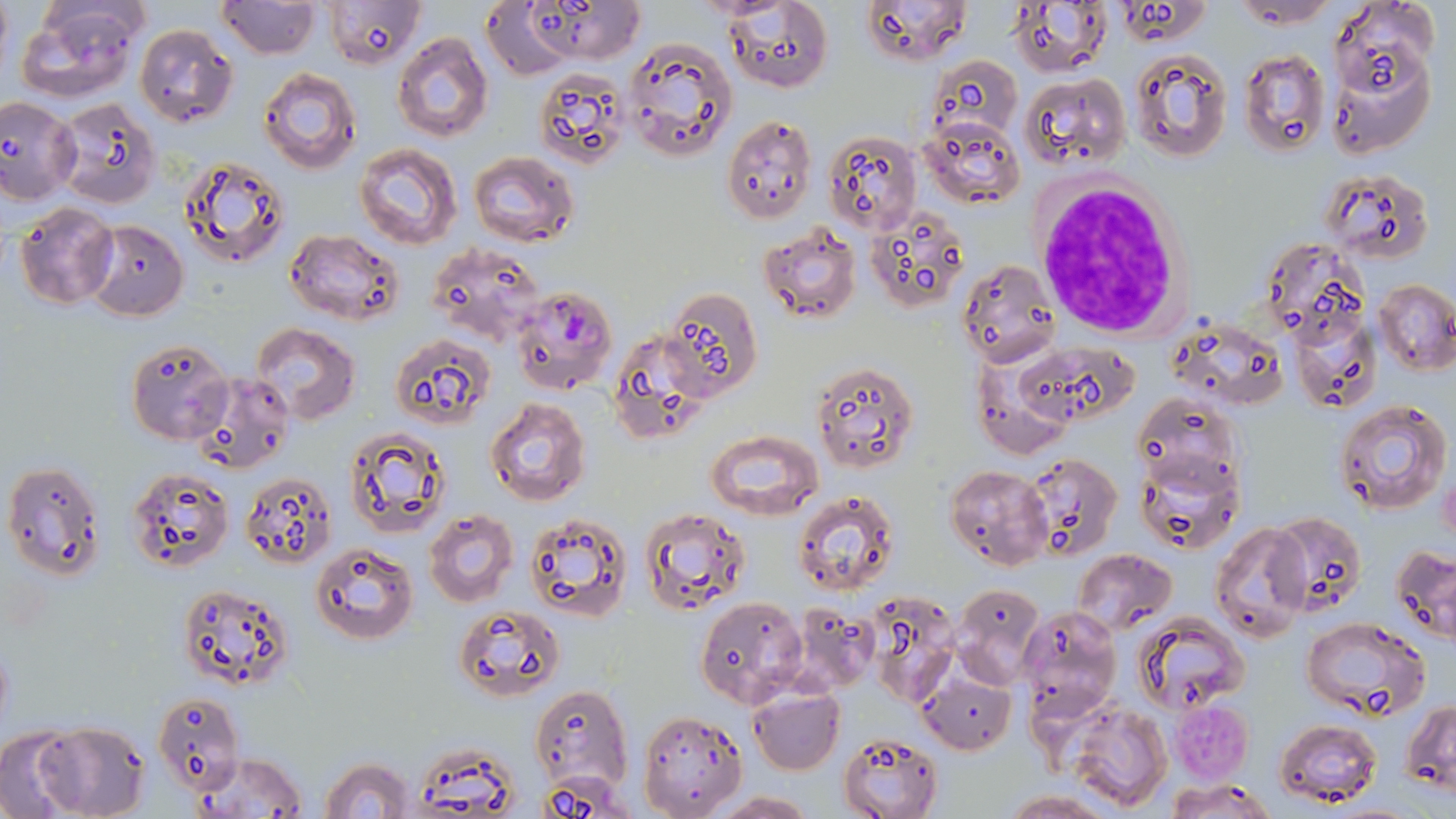

slide-level diagnosis = Plasmodium falciparum
field of view = one of a larger specimen
magnification = 1000x
preparation = thin blood smear
platelet locations = approximate bounding boxes as (x1, y1, x2, y2) in pixels: (1168, 698, 1255, 783)
modality = light microscopy
Plasmodium falciparum-infected red blood cell locations = approximate bounding boxes as (x1, y1, x2, y2) in pixels: (512, 285, 618, 393)
stain = May-Grünwald-Giemsa
white blood cell locations = approximate bounding boxes as (x1, y1, x2, y2) in pixels: (1023, 168, 1195, 349)
image size = 1456×819 pixels
uninfected red blood cell locations = approximate bounding boxes as (x1, y1, x2, y2) in pixels: (217, 0, 320, 59), (326, 0, 427, 70), (530, 0, 642, 64), (861, 0, 973, 67), (1231, 0, 1340, 28), (1009, 1, 1111, 78), (15, 2, 149, 103), (725, 2, 832, 91), (482, 3, 573, 79), (1331, 3, 1436, 105), (134, 24, 238, 127), (392, 33, 493, 142), (620, 37, 736, 163), (1127, 48, 1231, 164), (1239, 51, 1329, 158), (929, 56, 1022, 142), (258, 68, 360, 172), (533, 73, 631, 171), (1020, 73, 1132, 171), (0, 95, 80, 205), (54, 99, 160, 209), (919, 115, 1026, 210), (720, 116, 817, 224), (821, 128, 922, 236), (355, 143, 460, 249), (470, 150, 577, 249), (180, 157, 291, 267), (1322, 169, 1436, 266), (12, 201, 120, 310), (864, 209, 970, 314), (85, 219, 189, 320), (757, 220, 861, 325), (283, 227, 402, 324), (427, 242, 543, 345), (958, 257, 1060, 365), (1373, 278, 1456, 375), (659, 286, 761, 400), (1289, 313, 1380, 414), (1169, 317, 1286, 413), (251, 324, 360, 422), (388, 334, 496, 427), (126, 339, 231, 444), (1008, 342, 1137, 434), (809, 359, 919, 472), (191, 372, 296, 477), (485, 397, 591, 506), (1334, 398, 1452, 518), (343, 428, 449, 538), (706, 430, 823, 521), (1132, 448, 1244, 556), (1022, 452, 1122, 562), (1, 459, 106, 579), (945, 465, 1052, 569), (126, 469, 234, 571), (240, 472, 338, 568), (792, 491, 900, 598), (639, 506, 750, 615), (424, 510, 518, 607), (523, 510, 633, 623), (1268, 510, 1367, 614), (1211, 522, 1312, 641), (312, 544, 417, 644), (1392, 544, 1456, 643), (1074, 549, 1176, 632), (178, 582, 294, 689), (951, 582, 1045, 686), (868, 595, 963, 707), (696, 596, 808, 707), (789, 601, 879, 696), (452, 604, 565, 703), (1019, 605, 1120, 719), (1134, 613, 1249, 714), (1302, 617, 1430, 718), (917, 672, 1015, 756), (529, 685, 634, 798), (747, 688, 844, 775), (153, 691, 245, 794), (1062, 699, 1171, 812), (1404, 700, 1456, 794), (638, 710, 747, 819), (1274, 717, 1384, 806), (30, 722, 151, 819), (0, 730, 82, 817), (838, 732, 943, 818), (412, 743, 524, 815), (195, 753, 311, 817), (318, 755, 416, 819), (1165, 778, 1278, 818), (1002, 791, 1116, 819), (710, 793, 818, 818)